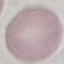

result: no malaria parasites seen
image_type: automatically extracted cell patch, resized to 64 × 64 pixels
capture: smartphone camera at the microscope eyepiece
stain: Giemsa
preparation: thin blood smear